Assess this cell for malaria.
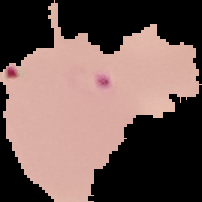
Parasitized.

image_type: segmented cell region with the area outside set to black
image_size: 202×202 pixels
preparation: thin blood film